Report the malaria status of this cell.
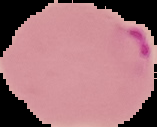

Parasitized.

Summary:
  - Image size: 157×127 pixels
  - Preparation: thin blood smear
  - Image type: segmented cell region on a black background